Identify the cell.
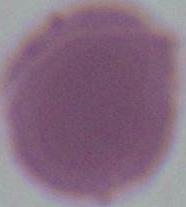
An erythrocyte.

Summary:
  - Modality: photomicrograph
  - Magnification: 1000x